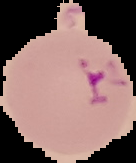
malaria_status: parasitized
preparation: thin blood film
image_type: segmented cell region with the area outside set to black
image_size: 136×163 pixels